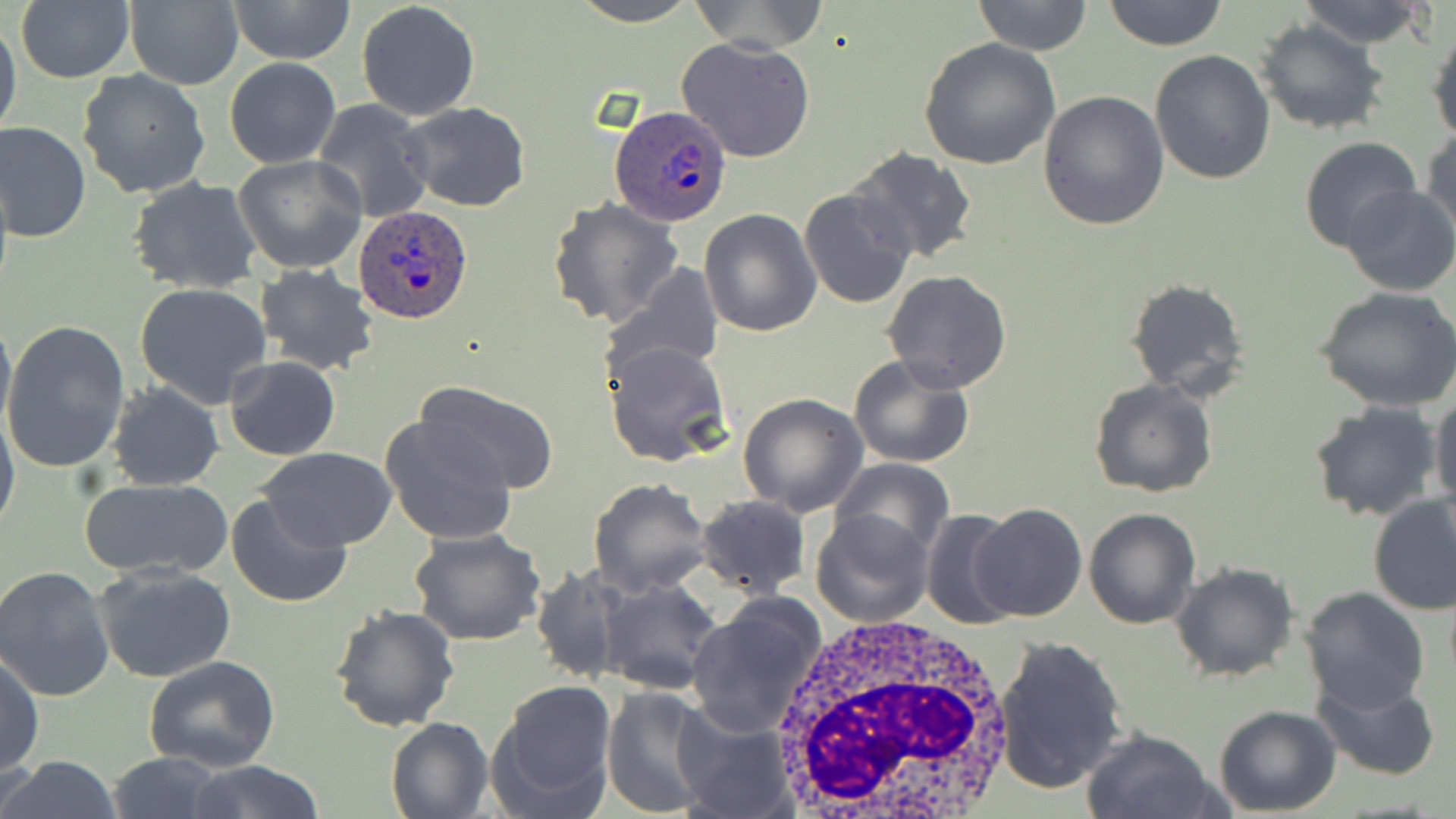

Plasmodium ovale-infected red blood cell locations = approximate bounding boxes as named x1/y1/x2/y2 corners in pixels: (x1=611, y1=107, x2=731, y2=224), (x1=355, y1=204, x2=473, y2=322)
slide-level diagnosis = Plasmodium ovale
uninfected red blood cell locations = approximate bounding boxes as named x1/y1/x2/y2 corners in pixels: (x1=15, y1=0, x2=135, y2=84), (x1=226, y1=0, x2=357, y2=64), (x1=357, y1=0, x2=481, y2=121), (x1=570, y1=0, x2=699, y2=26), (x1=688, y1=0, x2=830, y2=52), (x1=971, y1=0, x2=1093, y2=56), (x1=1102, y1=0, x2=1227, y2=50), (x1=1296, y1=0, x2=1434, y2=49), (x1=123, y1=1, x2=242, y2=90), (x1=0, y1=16, x2=21, y2=144), (x1=1254, y1=18, x2=1389, y2=136), (x1=1428, y1=20, x2=1456, y2=146), (x1=677, y1=38, x2=817, y2=163), (x1=919, y1=39, x2=1062, y2=172), (x1=1150, y1=48, x2=1276, y2=184), (x1=224, y1=58, x2=340, y2=168), (x1=76, y1=68, x2=210, y2=200), (x1=1038, y1=90, x2=1169, y2=230), (x1=312, y1=100, x2=433, y2=222), (x1=401, y1=103, x2=530, y2=212), (x1=1, y1=120, x2=92, y2=244), (x1=1422, y1=126, x2=1456, y2=246), (x1=1298, y1=137, x2=1422, y2=254), (x1=845, y1=146, x2=978, y2=265), (x1=234, y1=155, x2=368, y2=275), (x1=128, y1=178, x2=263, y2=295), (x1=1340, y1=186, x2=1456, y2=297), (x1=798, y1=188, x2=917, y2=308), (x1=546, y1=198, x2=684, y2=329), (x1=698, y1=209, x2=822, y2=335), (x1=603, y1=260, x2=725, y2=379), (x1=255, y1=265, x2=380, y2=378), (x1=882, y1=269, x2=1013, y2=392), (x1=1124, y1=278, x2=1250, y2=399), (x1=136, y1=281, x2=273, y2=409), (x1=1314, y1=286, x2=1456, y2=412), (x1=0, y1=310, x2=15, y2=435), (x1=2, y1=320, x2=132, y2=473), (x1=601, y1=339, x2=731, y2=468), (x1=848, y1=354, x2=976, y2=468), (x1=225, y1=356, x2=339, y2=460), (x1=1088, y1=377, x2=1218, y2=497), (x1=418, y1=380, x2=561, y2=492), (x1=106, y1=382, x2=225, y2=492), (x1=1428, y1=390, x2=1456, y2=514), (x1=738, y1=393, x2=869, y2=517), (x1=1308, y1=400, x2=1442, y2=521), (x1=0, y1=402, x2=20, y2=540), (x1=378, y1=413, x2=521, y2=546), (x1=257, y1=446, x2=399, y2=551), (x1=831, y1=457, x2=954, y2=561), (x1=78, y1=478, x2=233, y2=578), (x1=588, y1=478, x2=713, y2=598), (x1=225, y1=492, x2=353, y2=609), (x1=1368, y1=493, x2=1455, y2=614), (x1=695, y1=494, x2=812, y2=598), (x1=970, y1=503, x2=1087, y2=621), (x1=1084, y1=507, x2=1201, y2=629), (x1=920, y1=508, x2=1020, y2=631), (x1=809, y1=509, x2=933, y2=628), (x1=409, y1=528, x2=548, y2=646), (x1=93, y1=562, x2=237, y2=684), (x1=1170, y1=563, x2=1295, y2=682), (x1=531, y1=564, x2=629, y2=686), (x1=1, y1=566, x2=117, y2=702), (x1=599, y1=577, x2=724, y2=697), (x1=1299, y1=586, x2=1429, y2=714), (x1=686, y1=596, x2=828, y2=735), (x1=328, y1=604, x2=460, y2=734), (x1=994, y1=633, x2=1128, y2=795), (x1=1, y1=652, x2=44, y2=777), (x1=144, y1=655, x2=281, y2=771), (x1=1312, y1=677, x2=1441, y2=780), (x1=487, y1=681, x2=618, y2=816), (x1=601, y1=686, x2=720, y2=817), (x1=1214, y1=705, x2=1341, y2=816), (x1=671, y1=708, x2=795, y2=818), (x1=386, y1=717, x2=493, y2=819), (x1=1079, y1=727, x2=1223, y2=819), (x1=106, y1=752, x2=227, y2=819), (x1=0, y1=758, x2=123, y2=819), (x1=180, y1=761, x2=327, y2=819)
modality = optical microscopy
image size = 1456×819 pixels
white blood cell locations = approximate bounding boxes as named x1/y1/x2/y2 corners in pixels: (x1=769, y1=610, x2=1016, y2=819)
magnification = 1000x
field of view = single
stain = May-Grünwald-Giemsa
preparation = thin blood film